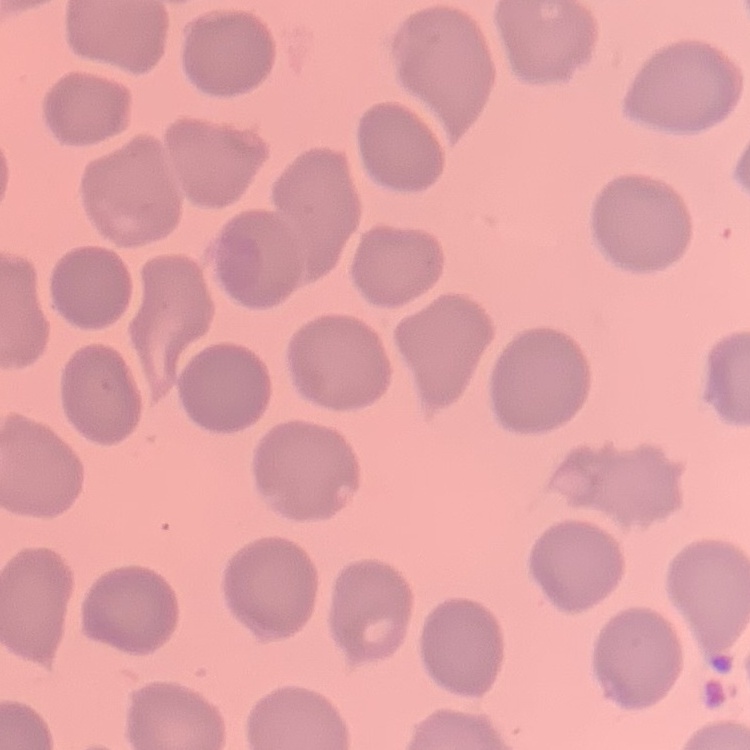
Summary:
  - Erythrocyte morphology: no rouleaux formation
  - Preparation: thin blood smear
  - Image type: one tile cut from a larger photomicrograph
  - Stain: Field's or Giemsa